State which parasite is depicted.
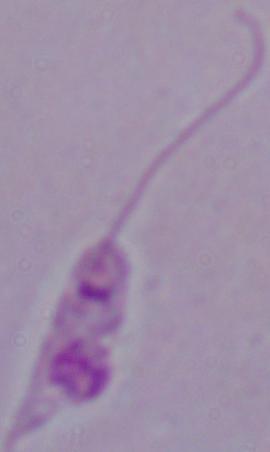

This is Leishmania.

Photomicrograph. Captured at 1000x magnification.